Assess this cell for malaria.
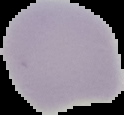

It is uninfected.

From a thin blood film. Image is 124×115 pixels. Cell region segmented out of the field of view; the surrounding area is masked to black.